State which parasite is depicted.
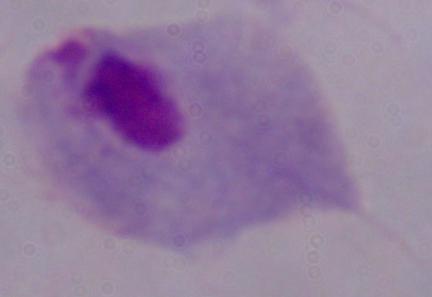

This is a trichomonad.

Summary:
  - Magnification: 1000x
  - Modality: micrograph